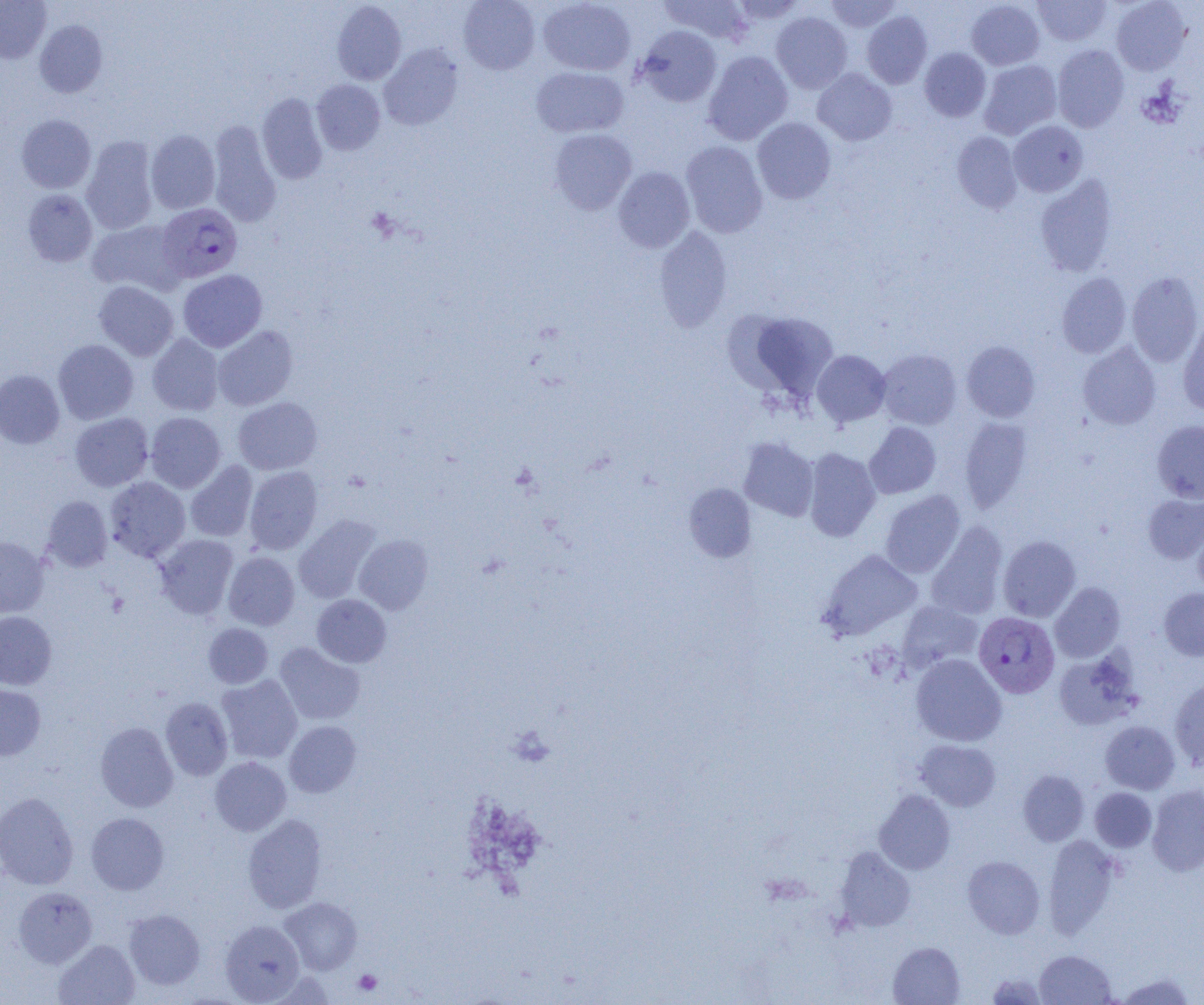 Approximate bounding boxes as named x1/y1/x2/y2 corners in pixels. Platelet locations: (x1=353, y1=969, x2=382, y2=995). Plasmodium vivax-infected red blood cell locations: (x1=157, y1=203, x2=243, y2=282), (x1=974, y1=612, x2=1059, y2=698). Uninfected red blood cell locations: (x1=0, y1=0, x2=51, y2=63), (x1=458, y1=0, x2=540, y2=74), (x1=538, y1=0, x2=636, y2=76), (x1=659, y1=0, x2=754, y2=46), (x1=730, y1=0, x2=809, y2=25), (x1=825, y1=0, x2=902, y2=33), (x1=966, y1=0, x2=1045, y2=70), (x1=1033, y1=0, x2=1111, y2=47), (x1=1111, y1=0, x2=1191, y2=75), (x1=332, y1=1, x2=406, y2=85), (x1=861, y1=10, x2=932, y2=89), (x1=771, y1=12, x2=852, y2=94), (x1=35, y1=20, x2=108, y2=97), (x1=635, y1=26, x2=722, y2=107), (x1=379, y1=44, x2=463, y2=130), (x1=1052, y1=44, x2=1129, y2=132), (x1=919, y1=47, x2=991, y2=122), (x1=703, y1=50, x2=793, y2=145), (x1=695, y1=53, x2=780, y2=240), (x1=978, y1=59, x2=1061, y2=139), (x1=531, y1=66, x2=629, y2=138), (x1=812, y1=68, x2=897, y2=145), (x1=311, y1=79, x2=385, y2=155), (x1=257, y1=93, x2=328, y2=184), (x1=17, y1=114, x2=96, y2=192), (x1=752, y1=117, x2=836, y2=204), (x1=208, y1=120, x2=281, y2=227), (x1=1008, y1=120, x2=1088, y2=197), (x1=549, y1=128, x2=637, y2=214), (x1=146, y1=129, x2=220, y2=214), (x1=952, y1=131, x2=1023, y2=213), (x1=81, y1=136, x2=159, y2=235), (x1=680, y1=140, x2=768, y2=238), (x1=613, y1=166, x2=695, y2=253), (x1=1035, y1=175, x2=1118, y2=277), (x1=22, y1=189, x2=97, y2=267), (x1=87, y1=219, x2=185, y2=295), (x1=654, y1=226, x2=733, y2=332), (x1=178, y1=269, x2=267, y2=352), (x1=1127, y1=271, x2=1203, y2=367), (x1=1057, y1=272, x2=1132, y2=358), (x1=93, y1=281, x2=178, y2=361), (x1=735, y1=309, x2=839, y2=402), (x1=1177, y1=318, x2=1204, y2=415), (x1=212, y1=325, x2=298, y2=410), (x1=147, y1=333, x2=224, y2=416), (x1=53, y1=339, x2=138, y2=424), (x1=961, y1=341, x2=1041, y2=422), (x1=1078, y1=342, x2=1161, y2=430), (x1=876, y1=349, x2=962, y2=430), (x1=812, y1=350, x2=891, y2=427), (x1=0, y1=369, x2=65, y2=449), (x1=233, y1=397, x2=322, y2=475), (x1=145, y1=412, x2=226, y2=493), (x1=70, y1=413, x2=153, y2=491), (x1=959, y1=418, x2=1032, y2=514), (x1=1152, y1=420, x2=1204, y2=503), (x1=864, y1=422, x2=941, y2=499), (x1=738, y1=437, x2=819, y2=521), (x1=803, y1=448, x2=881, y2=541), (x1=185, y1=461, x2=258, y2=542), (x1=244, y1=466, x2=322, y2=554), (x1=105, y1=476, x2=190, y2=562), (x1=684, y1=483, x2=756, y2=562), (x1=880, y1=490, x2=965, y2=578), (x1=1143, y1=494, x2=1204, y2=563), (x1=41, y1=495, x2=112, y2=571), (x1=294, y1=514, x2=381, y2=603), (x1=926, y1=521, x2=1008, y2=620), (x1=1193, y1=521, x2=1204, y2=597), (x1=155, y1=534, x2=238, y2=619), (x1=354, y1=534, x2=433, y2=615), (x1=0, y1=536, x2=49, y2=618), (x1=998, y1=536, x2=1080, y2=621), (x1=818, y1=549, x2=922, y2=641), (x1=223, y1=552, x2=299, y2=630), (x1=1050, y1=582, x2=1125, y2=663), (x1=1159, y1=587, x2=1204, y2=661), (x1=312, y1=594, x2=391, y2=667), (x1=897, y1=600, x2=983, y2=672), (x1=0, y1=611, x2=56, y2=690), (x1=203, y1=623, x2=273, y2=688), (x1=274, y1=642, x2=364, y2=725), (x1=1053, y1=650, x2=1141, y2=731), (x1=911, y1=654, x2=1006, y2=746), (x1=216, y1=675, x2=303, y2=763), (x1=1169, y1=677, x2=1204, y2=770), (x1=0, y1=682, x2=46, y2=761), (x1=160, y1=697, x2=233, y2=781), (x1=284, y1=720, x2=361, y2=797), (x1=1100, y1=720, x2=1180, y2=794), (x1=95, y1=722, x2=178, y2=812), (x1=914, y1=739, x2=1001, y2=811), (x1=210, y1=757, x2=291, y2=836), (x1=1018, y1=770, x2=1089, y2=846), (x1=1147, y1=785, x2=1204, y2=876), (x1=1090, y1=787, x2=1157, y2=852), (x1=874, y1=789, x2=955, y2=875), (x1=0, y1=792, x2=79, y2=889), (x1=85, y1=812, x2=169, y2=895), (x1=243, y1=814, x2=327, y2=913), (x1=1043, y1=834, x2=1121, y2=939), (x1=834, y1=846, x2=915, y2=931), (x1=962, y1=855, x2=1045, y2=939), (x1=13, y1=886, x2=97, y2=968), (x1=280, y1=897, x2=362, y2=974), (x1=124, y1=909, x2=205, y2=990), (x1=220, y1=920, x2=305, y2=1004), (x1=53, y1=939, x2=140, y2=1005), (x1=888, y1=941, x2=965, y2=1004), (x1=1034, y1=950, x2=1116, y2=1004), (x1=986, y1=972, x2=1048, y2=1004), (x1=1116, y1=972, x2=1196, y2=1004). Slide-level diagnosis: Plasmodium vivax. Thin blood smear. Single field of view. Light microscopy. 1000x magnification. Image is 1204×1005 pixels.